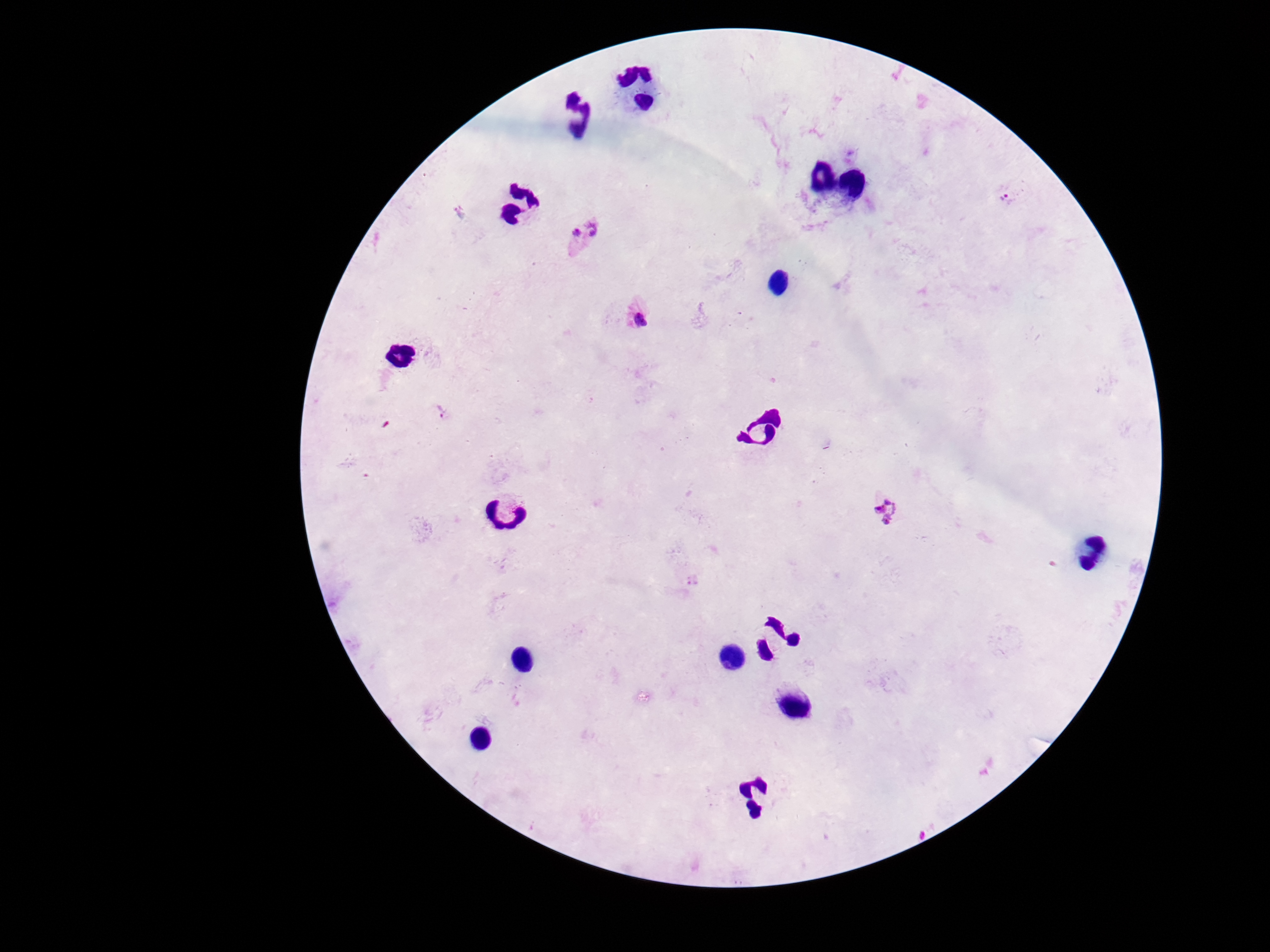
patient_malaria_status: infected
image_size: 1270×952 pixels
plasmodium_parasite_locations: 'approximate centers as (x, y) in pixels: (1010, 194), (581, 235), (639, 315), (441, 413), (885, 508)'
capture: smartphone camera through the microscope eyepiece
magnification: 100x
preparation: thick blood film
stain: Giemsa
field_of_view: single